Identify the preparation type.
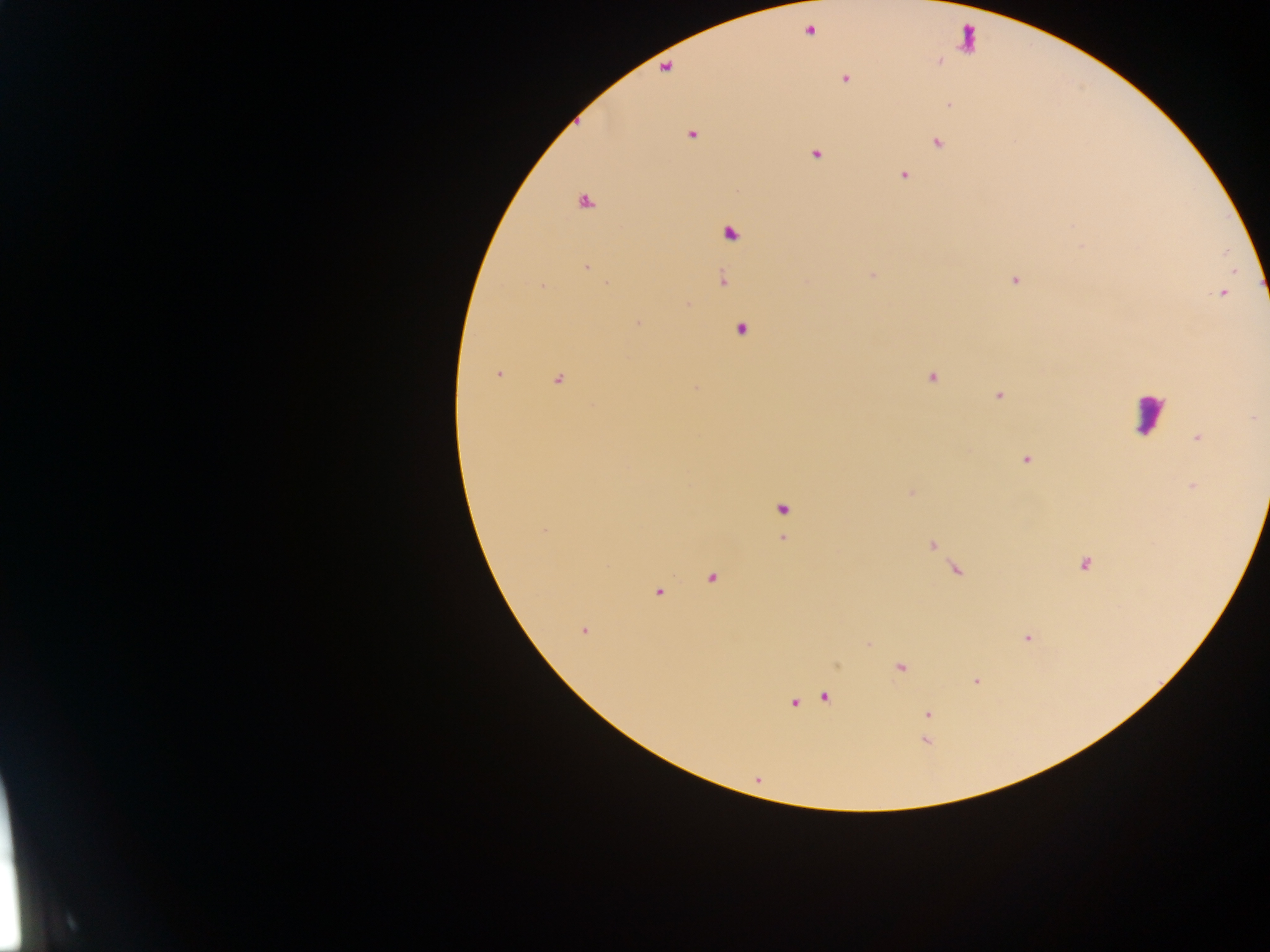
This is a thick smear.

Approximate centers as x y in pixels. Malaria parasite locations: 809 30; 939 60; 665 67; 844 78; 949 104; 691 133; 936 142; 815 153; 903 175; 583 201; 729 232; 586 267; 873 275; 1014 279; 722 280; 542 286; 1222 293; 687 304; 638 323; 740 330; 499 374; 931 376; 558 379; 696 388; 998 394; 1197 437; 1026 458; 1193 485; 911 493; 782 509; 544 530; 782 539; 931 544; 1084 564; 956 569; 711 576; 658 590; 582 630; 1026 637; 868 643; 837 664; 900 667; 976 681; 824 696; 794 702; 927 714; 925 739; 758 780. Leukocyte locations: 967 39; 1148 413. Sample from Ghana. Image is 1270×952 pixels. Photographed through a microscope with a mobile-phone camera. Single field of view.